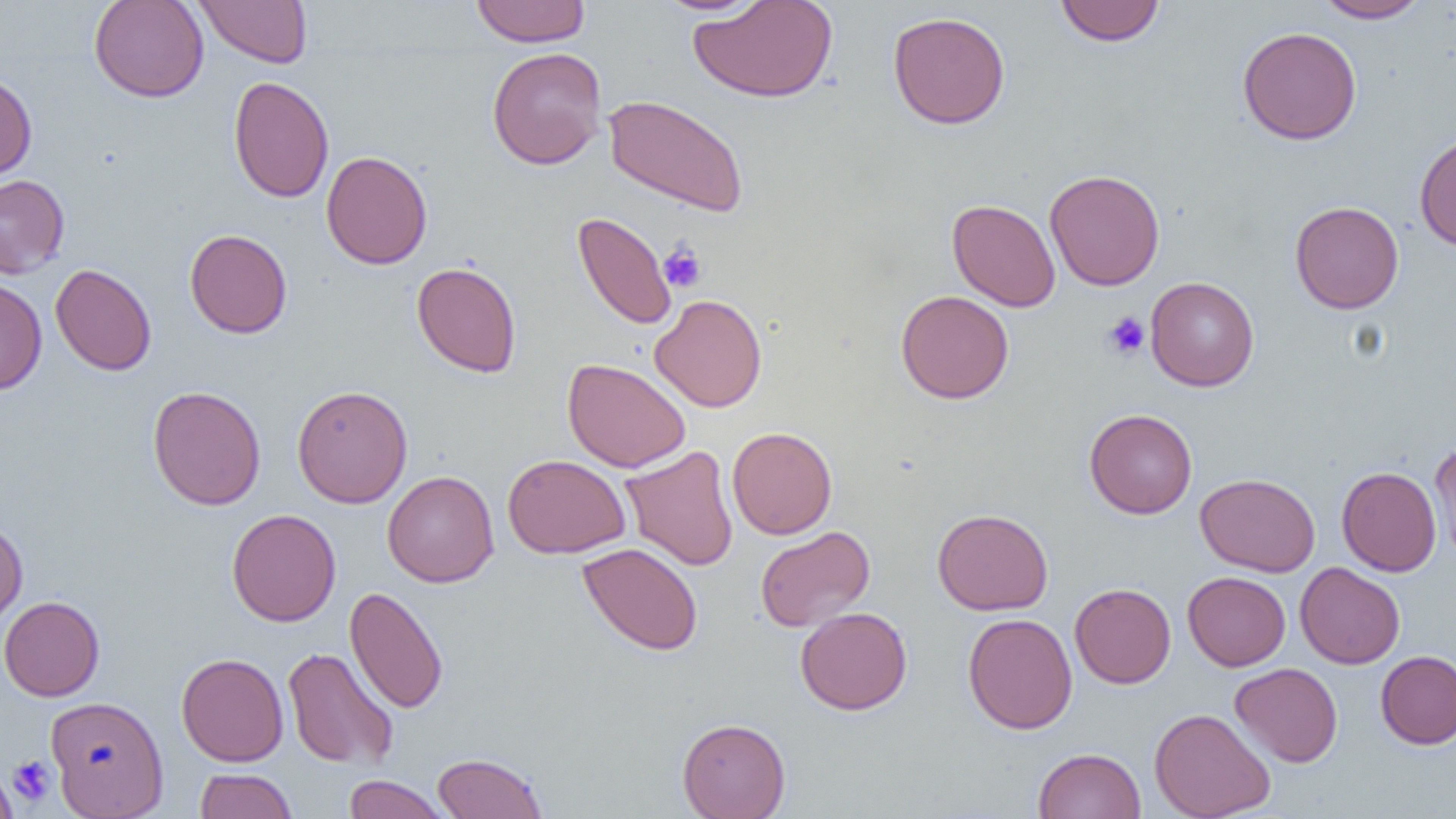
slide-level diagnosis = negative for blood parasites
image size = 1456×819 pixels
modality = optical microscopy
preparation = thin blood smear
field of view = one of a larger specimen
magnification = 1000x
platelet locations = approximate bounding boxes as (x1,y1)-(x2,y2) corner pairs in pixels: (658,241)-(707,292), (1102,312)-(1150,360), (8,755)-(57,807)
uninfected red blood cell locations = approximate bounding boxes as (x1,y1)-(x2,y2) corner pairs in pixels: (89,0)-(209,102), (195,0)-(313,68), (470,0)-(591,47), (654,0)-(769,16), (687,0)-(838,103), (1314,0)-(1429,23), (1055,1)-(1165,46), (887,11)-(1011,129), (1237,26)-(1362,145), (487,46)-(607,170), (0,70)-(37,182), (228,75)-(334,203), (604,94)-(749,216), (1414,131)-(1456,251), (321,151)-(432,269), (1044,169)-(1165,290), (0,174)-(70,279), (947,199)-(1061,312), (1289,200)-(1404,314), (573,212)-(677,330), (184,229)-(292,338), (411,261)-(522,377), (50,263)-(157,376), (1146,276)-(1259,391), (0,277)-(47,395), (896,290)-(1014,404), (649,294)-(768,412), (561,358)-(691,473), (148,385)-(266,510), (291,385)-(413,507), (1084,408)-(1197,519), (727,426)-(838,540), (1429,440)-(1456,563), (620,445)-(739,571), (502,454)-(630,558), (1337,466)-(1441,577), (382,470)-(499,587), (1195,472)-(1321,577), (227,508)-(341,626), (932,508)-(1053,615), (0,519)-(28,632), (755,525)-(875,632), (577,542)-(703,655), (1294,562)-(1405,669), (1183,571)-(1290,671), (1069,583)-(1176,689), (345,586)-(448,714), (0,596)-(105,701), (795,607)-(912,715), (962,612)-(1078,734), (283,647)-(399,770), (1376,650)-(1456,749), (176,652)-(289,766), (1230,662)-(1343,767), (45,695)-(169,818), (1149,707)-(1276,819), (677,717)-(791,819), (1033,747)-(1146,818), (432,752)-(547,819), (0,764)-(19,819), (194,768)-(299,819), (343,775)-(449,818)